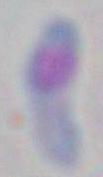
modality = photomicrograph
identification = Toxoplasma gondii
magnification = 1000x